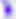

Summary:
  - Magnification: 400x
  - Modality: photomicrograph
  - Identification: Toxoplasma gondii